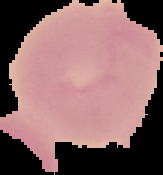
preparation = thin blood smear
image type = cell region segmented out of the field of view; surrounding area masked to black
malaria status = uninfected
image size = 163×175 pixels